Classify this cell by malaria status.
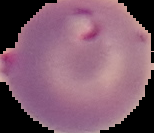

Parasitized.

image type = segmented cell region on a black background
image size = 154×133 pixels
preparation = thin blood film